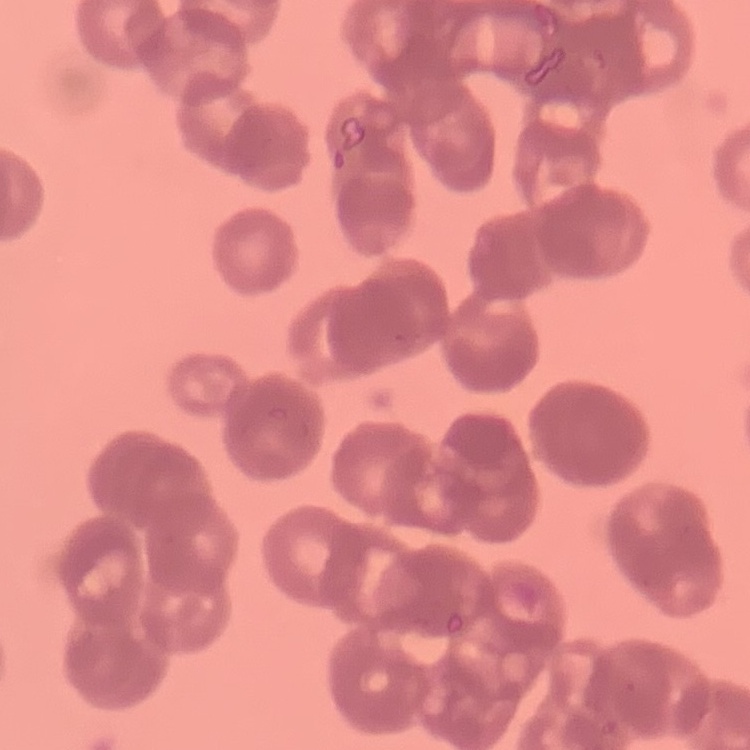

Summary:
  - Erythrocyte morphology: rouleaux formation
  - Stain: Field's or Giemsa
  - Preparation: thin blood smear
  - Image type: one tile cut from a larger photomicrograph